Point out each leukocyte.
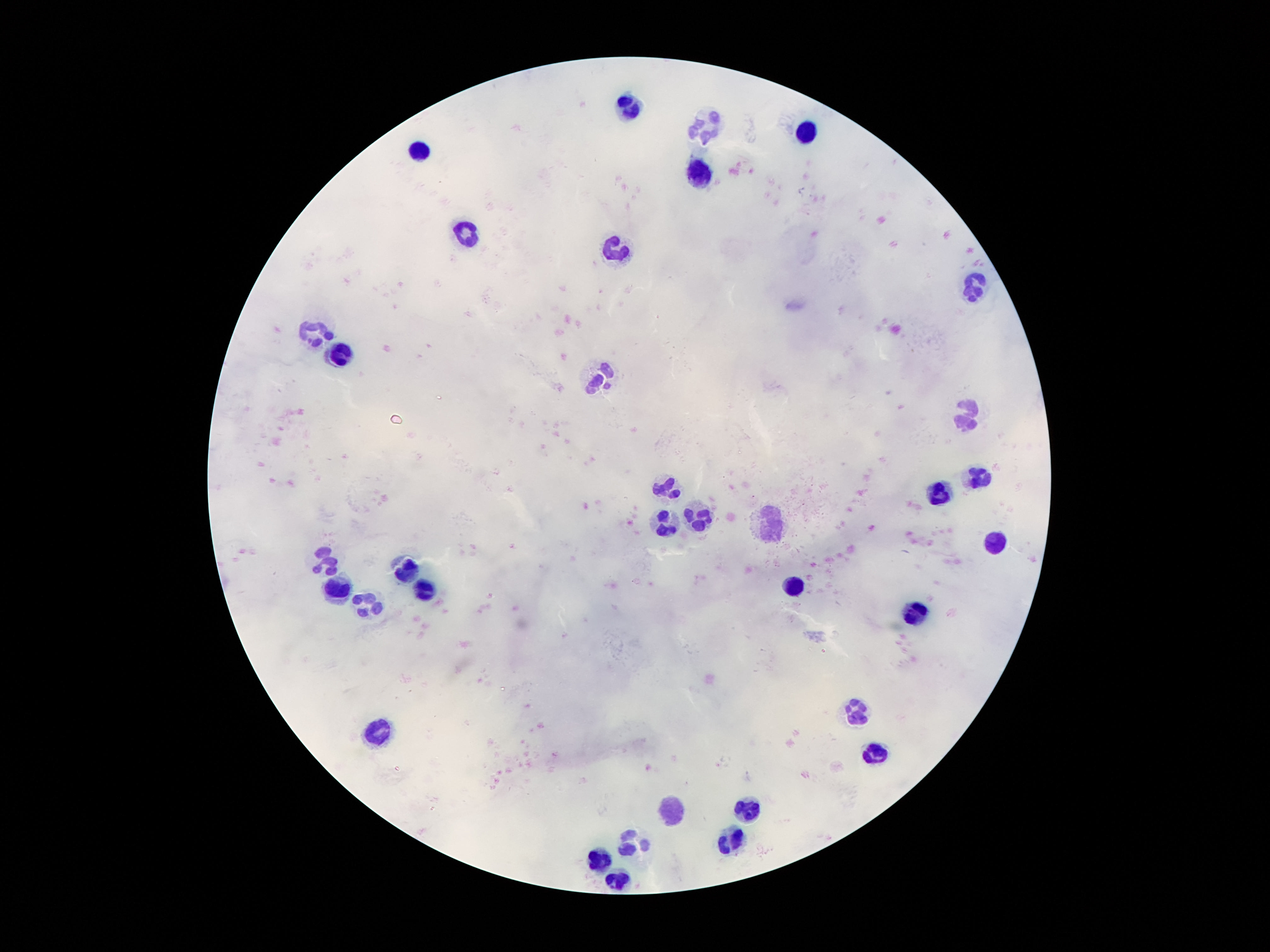
Approximate centers as {x, y} in pixels.
Leukocytes: {631, 107}, {703, 128}, {806, 133}, {419, 150}, {699, 173}, {468, 232}, {615, 253}, {975, 283}, {314, 332}, {339, 355}, {599, 380}, {965, 410}, {982, 477}, {666, 490}, {939, 495}, {697, 518}, {668, 523}, {771, 527}, {996, 541}, {330, 557}, {408, 567}, {791, 585}, {337, 589}, {427, 589}, {367, 604}, {916, 614}, {857, 708}, {378, 731}, {873, 752}, {674, 809}, {748, 809}, {634, 841}, {732, 841}, {603, 858}, {615, 879}.

Summary:
  - Stain: Giemsa
  - Patient malaria status: negative
  - Preparation: thick blood film
  - Magnification: 100x
  - Image size: 1270×952 pixels
  - Capture: smartphone camera through the microscope eyepiece
  - Field of view: one from this slide